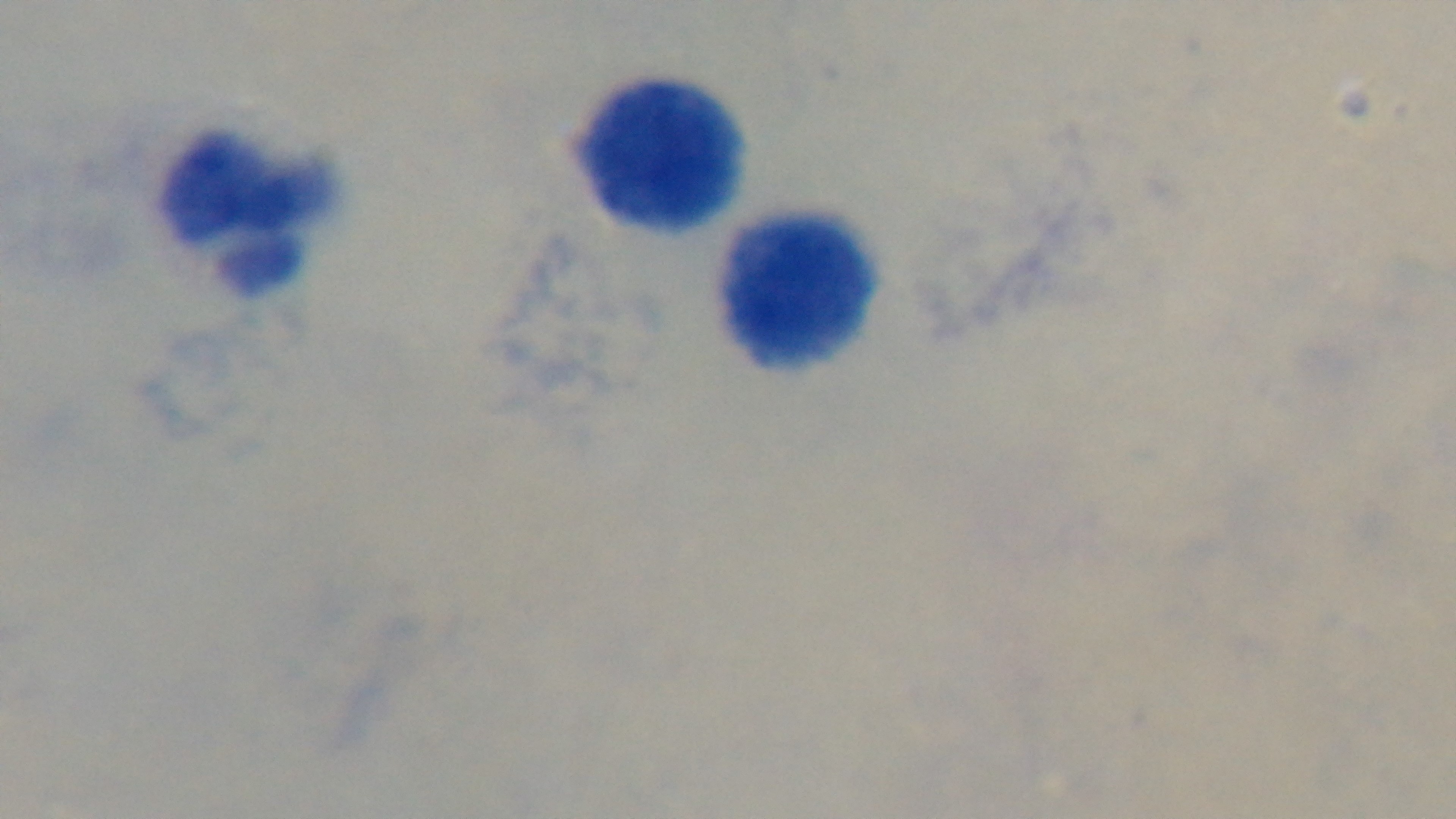
stain = Giemsa
capture = mounted 4K digital camera
malaria status = uninfected
modality = light microscopy
objective = 100x oil immersion
field of view = one from the slide
preparation = thick